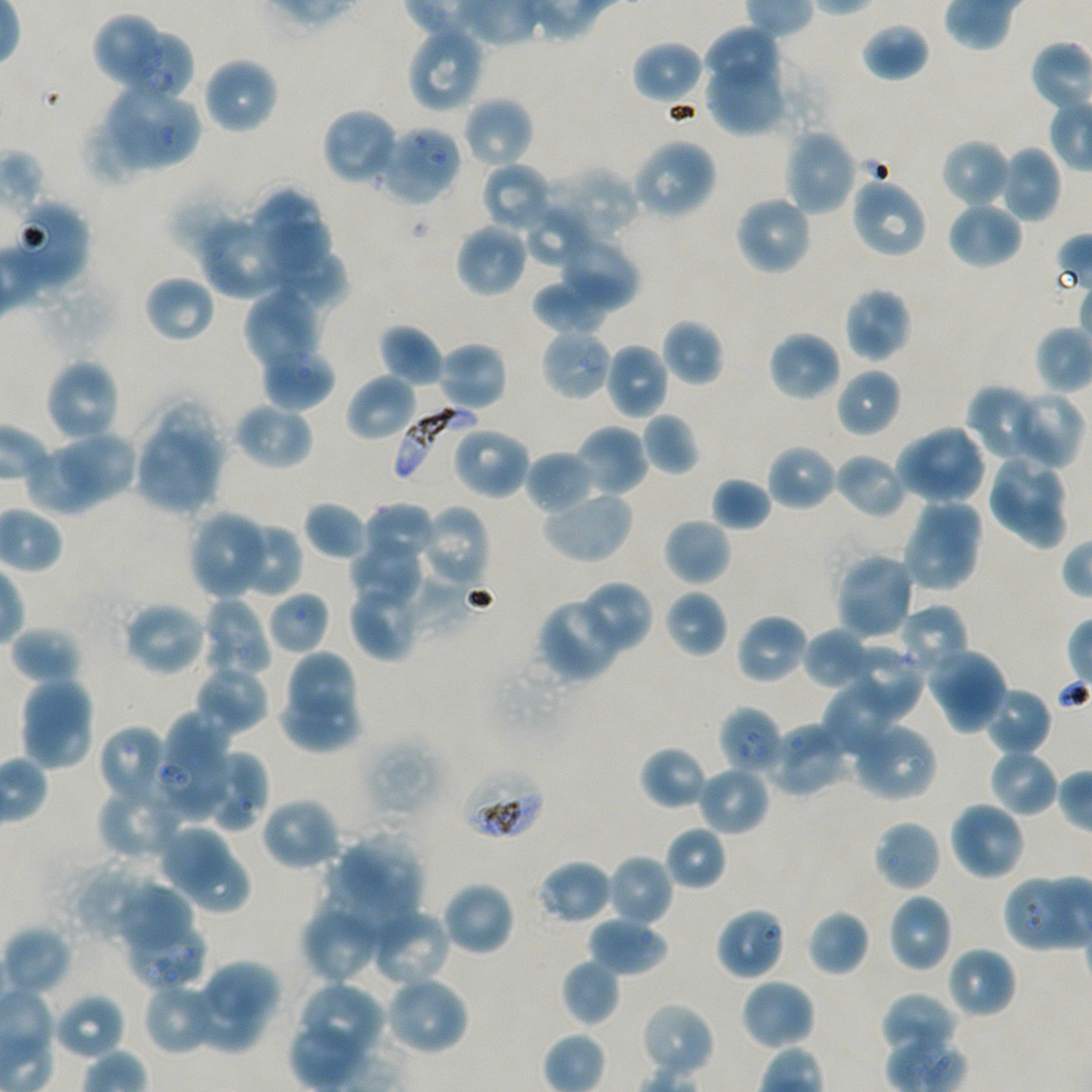
Not every red blood cell is marked. A life-cycle stage — or a range of stages, where the recorded stages span more than one — follows each staged infected red blood cell.
stain: Giemsa
donor_blood_group: A+/O+
locations_of_red_blood_cells_of_indeterminate_infection_status: 'approximate bounding boxes as {x1, y1, x2, y2} in pixels: {95, 15, 162, 88}, {125, 33, 194, 103}, {540, 327, 613, 402}, {156, 710, 230, 819}, {458, 766, 546, 843}, {126, 927, 208, 989}'
image_size: 1092×1092 pixels
culture: Plasmodium falciparum strain NF54, static, in vitro
objective: 100x, oil immersion, numerical aperture 1.45
preparation: thin blood smear
field_of_view: one from this slide
locations_of_infected_red_blood_cells: 'approximate bounding boxes as {x1, y1, x2, y2} in pixels: {394, 405, 477, 488}; {718, 706, 784, 778} early ring to early trophozoite'
locations_of_uninfected_red_blood_cells: 'approximate bounding boxes as {x1, y1, x2, y2} in pixels: {860, 22, 930, 83}, {405, 25, 485, 114}, {703, 26, 778, 83}, {632, 40, 705, 106}, {706, 54, 786, 136}, {202, 56, 279, 135}, {105, 84, 200, 172}, {462, 96, 534, 169}, {322, 107, 400, 187}, {82, 116, 153, 187}, {377, 125, 462, 206}, {783, 128, 858, 215}, {941, 138, 1012, 209}, {632, 139, 718, 221}, {995, 145, 1063, 223}, {481, 162, 553, 234}, {547, 164, 640, 241}, {850, 176, 928, 259}, {168, 183, 253, 259}, {248, 188, 322, 259}, {733, 194, 813, 276}, {10, 198, 91, 291}, {945, 200, 1023, 270}, {526, 204, 596, 269}, {199, 216, 295, 299}, {268, 217, 330, 270}, {455, 223, 529, 298}, {556, 230, 640, 312}, {268, 252, 347, 310}, {143, 274, 215, 343}, {532, 278, 612, 335}, {842, 286, 913, 363}, {244, 287, 323, 371}, {661, 318, 725, 386}, {380, 323, 444, 388}, {767, 329, 842, 403}, {435, 340, 509, 413}, {604, 342, 670, 420}, {260, 346, 335, 412}, {43, 358, 122, 443}, {835, 367, 902, 437}, {346, 372, 418, 443}, {966, 384, 1049, 465}, {1009, 390, 1085, 470}, {232, 401, 314, 471}, {642, 412, 699, 476}, {450, 424, 531, 500}, {575, 424, 649, 497}, {894, 424, 987, 505}, {134, 428, 215, 514}, {65, 431, 134, 500}, {28, 443, 105, 515}, {765, 443, 837, 512}, {524, 450, 596, 515}, {833, 452, 908, 519}, {986, 454, 1061, 527}, {711, 477, 771, 532}, {989, 484, 1068, 551}, {541, 489, 634, 564}, {916, 495, 982, 558}, {304, 500, 371, 560}, {363, 502, 435, 564}, {420, 505, 490, 589}, {189, 510, 272, 599}, {663, 517, 732, 587}, {228, 520, 304, 600}, {905, 522, 978, 592}, {350, 541, 422, 605}, {835, 551, 917, 640}, {354, 562, 475, 647}, {349, 580, 422, 661}, {575, 581, 653, 654}, {663, 589, 728, 659}, {267, 590, 331, 655}, {198, 597, 272, 680}, {536, 597, 623, 682}, {122, 600, 208, 677}, {896, 604, 970, 680}, {735, 613, 808, 686}, {10, 625, 83, 685}, {802, 627, 873, 691}, {844, 644, 923, 723}, {926, 645, 1008, 734}, {283, 651, 361, 736}, {194, 664, 270, 735}, {19, 676, 96, 771}, {822, 678, 907, 758}, {982, 687, 1053, 757}, {280, 688, 361, 752}, {767, 720, 849, 797}, {850, 720, 937, 801}, {98, 724, 169, 806}, {361, 737, 441, 824}, {639, 745, 710, 811}, {987, 747, 1059, 817}, {198, 748, 270, 833}, {696, 764, 771, 837}, {97, 784, 183, 861}, {260, 796, 342, 873}, {948, 800, 1026, 881}, {873, 819, 943, 893}, {158, 823, 230, 892}, {664, 825, 727, 891}, {340, 838, 422, 911}, {184, 848, 248, 913}, {606, 853, 674, 928}, {537, 859, 614, 926}, {84, 873, 161, 938}, {1005, 876, 1070, 950}, {440, 880, 516, 957}, {118, 883, 198, 962}, {887, 892, 953, 972}, {299, 904, 382, 985}, {369, 907, 453, 988}, {714, 907, 787, 981}, {807, 909, 871, 977}, {587, 915, 670, 976}, {1, 925, 72, 998}, {945, 945, 1017, 1019}, {560, 958, 620, 1027}, {209, 959, 282, 1018}, {382, 975, 470, 1057}, {740, 977, 816, 1051}, {142, 981, 221, 1055}, {193, 983, 264, 1053}, {298, 983, 385, 1066}, {880, 992, 959, 1057}, {53, 993, 126, 1061}, {639, 1002, 716, 1080}'